Classify this cell by malaria status.
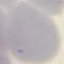

Uninfected.

Thin smear of blood. Giemsa stain. Photographed with a smartphone camera at the microscope eyepiece. Automatically extracted cell patch, resized to 64 × 64 pixels.